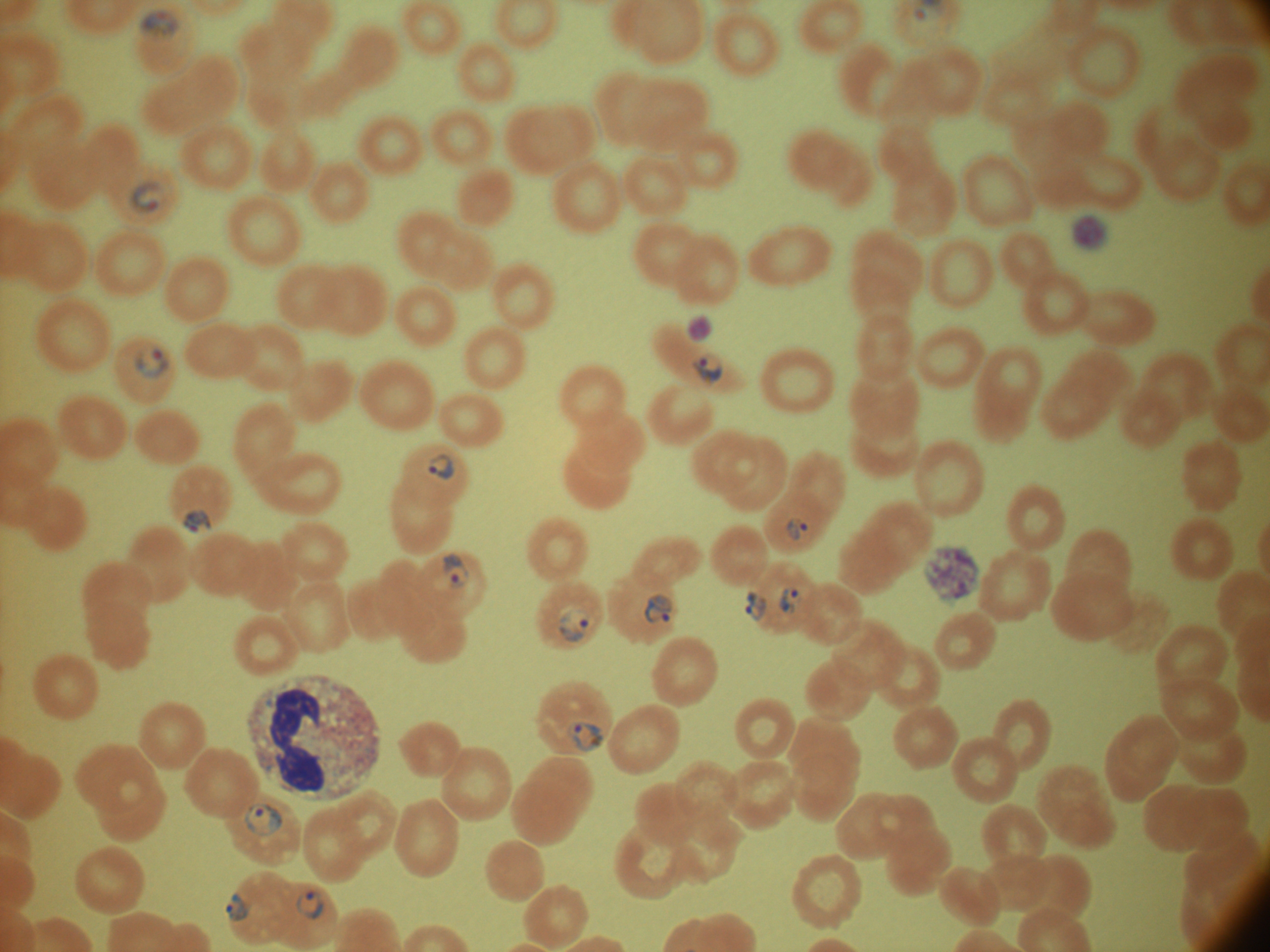
life-cycle stages among the annotated parasites = ring form, trophozoite
magnification = 100x
species = Plasmodium falciparum
ring form locations = approximate bounding boxes as [x1, y1, x2, y2] in pixels, from the source annotation, which is not necessarily exhaustive: [140, 8, 181, 41], [131, 181, 167, 214], [135, 348, 169, 379], [692, 354, 723, 388], [427, 453, 455, 480], [182, 509, 213, 533], [783, 517, 810, 542], [442, 553, 470, 589], [779, 587, 803, 614], [745, 591, 766, 622], [644, 593, 674, 624], [558, 605, 589, 643], [244, 803, 283, 835], [225, 892, 249, 922], [296, 892, 323, 920]
field of view = single
microscope = Leica DM2000 with built-in camera
trophozoite locations = approximate bounding boxes as [x1, y1, x2, y2] in pixels, from the source annotation, which is not necessarily exhaustive: [567, 720, 606, 754]
preparation = thin blood smear
image size = 1270×952 pixels
stain = Giemsa